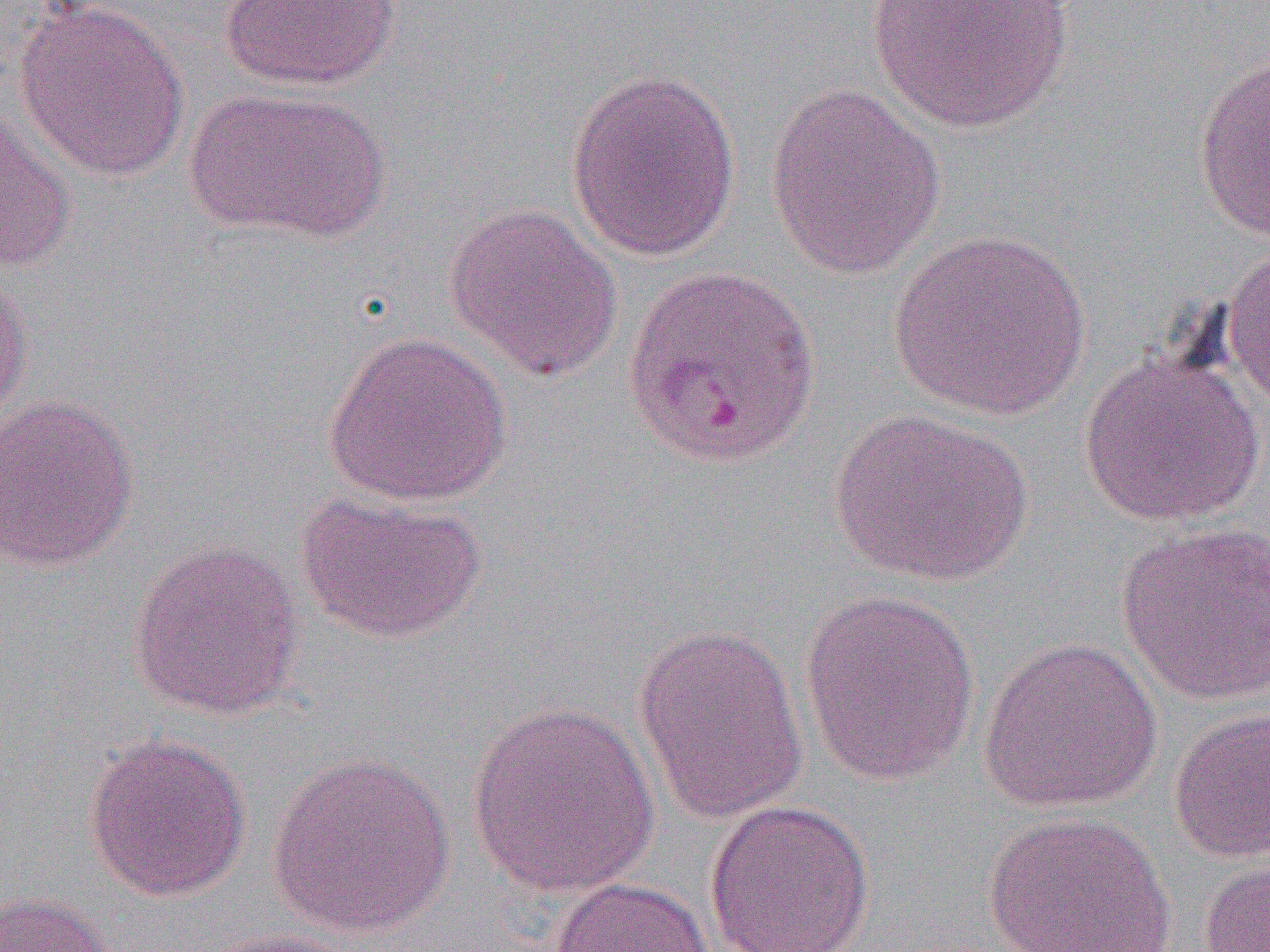

Summary:
  - Coordinate format: approximate bounding boxes as (x1, y1, x2, y2) in pixels
  - Uninfected red blood cell locations: (865, 0, 1075, 134), (219, 1, 400, 90), (13, 2, 190, 181), (1192, 48, 1270, 241), (564, 67, 742, 264), (764, 84, 946, 280), (187, 87, 387, 241), (0, 105, 79, 273), (444, 203, 623, 382), (888, 229, 1092, 419), (1223, 242, 1270, 415), (0, 264, 34, 430), (322, 330, 513, 507), (1079, 345, 1266, 527), (0, 393, 140, 572), (828, 407, 1035, 587), (293, 489, 488, 644), (1115, 522, 1270, 707), (127, 538, 306, 720), (798, 588, 982, 788), (632, 622, 810, 824), (978, 637, 1163, 813), (465, 701, 661, 898), (1169, 705, 1270, 864), (83, 733, 251, 902), (266, 750, 456, 939), (702, 799, 875, 952), (982, 811, 1177, 951), (1199, 857, 1270, 951), (548, 876, 714, 952), (0, 891, 117, 952), (190, 928, 368, 952)
  - Slide-level diagnosis: Plasmodium vivax
  - Image size: 1270×952 pixels
  - Modality: optical microscopy
  - Field of view: one of a larger specimen
  - Magnification: 1000x
  - Preparation: thin blood film